Locate every blood parasite and identify its species.
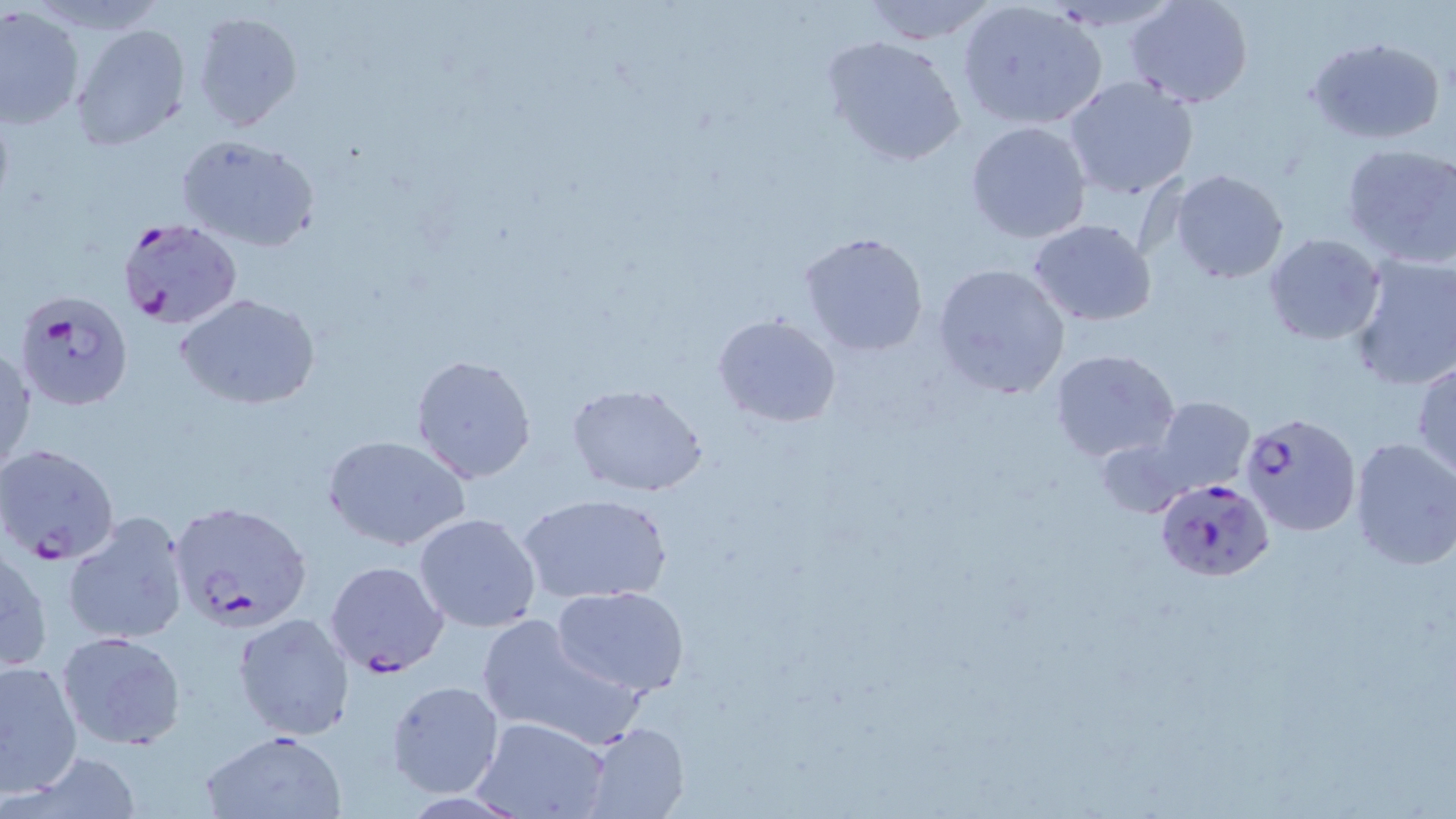
Approximate bounding boxes as named x1/y1/x2/y2 corners in pixels.
Plasmodium falciparum-infected red blood cells: (x1=113, y1=216, x2=243, y2=329), (x1=15, y1=288, x2=135, y2=411), (x1=1240, y1=413, x2=1361, y2=538), (x1=0, y1=442, x2=122, y2=565), (x1=1155, y1=478, x2=1273, y2=582), (x1=168, y1=500, x2=315, y2=635), (x1=324, y1=560, x2=449, y2=678).
No Plasmodium ovale, Plasmodium malariae, Plasmodium vivax, Babesia divergens, or Trypanosoma brucei observed.

Uninfected red blood cell locations: (x1=860, y1=0, x2=998, y2=43), (x1=1124, y1=1, x2=1254, y2=107), (x1=957, y1=4, x2=1105, y2=129), (x1=0, y1=5, x2=85, y2=128), (x1=189, y1=9, x2=303, y2=134), (x1=71, y1=23, x2=190, y2=152), (x1=824, y1=35, x2=967, y2=168), (x1=1305, y1=35, x2=1445, y2=144), (x1=1062, y1=75, x2=1198, y2=200), (x1=965, y1=120, x2=1092, y2=243), (x1=175, y1=133, x2=322, y2=254), (x1=1340, y1=141, x2=1456, y2=270), (x1=1171, y1=169, x2=1289, y2=283), (x1=1028, y1=220, x2=1158, y2=327), (x1=797, y1=231, x2=929, y2=358), (x1=1264, y1=233, x2=1384, y2=344), (x1=1348, y1=253, x2=1456, y2=392), (x1=932, y1=263, x2=1071, y2=400), (x1=175, y1=292, x2=321, y2=409), (x1=711, y1=313, x2=842, y2=427), (x1=1, y1=340, x2=35, y2=480), (x1=1049, y1=349, x2=1181, y2=465), (x1=408, y1=353, x2=538, y2=485), (x1=1411, y1=361, x2=1456, y2=478), (x1=565, y1=382, x2=710, y2=498), (x1=1149, y1=396, x2=1256, y2=497), (x1=323, y1=435, x2=471, y2=553), (x1=1097, y1=436, x2=1195, y2=519), (x1=1347, y1=437, x2=1456, y2=570), (x1=522, y1=493, x2=671, y2=606), (x1=63, y1=511, x2=190, y2=646), (x1=413, y1=513, x2=542, y2=634), (x1=0, y1=543, x2=51, y2=676), (x1=552, y1=585, x2=691, y2=698), (x1=232, y1=612, x2=354, y2=743), (x1=475, y1=613, x2=639, y2=749), (x1=57, y1=631, x2=186, y2=751), (x1=0, y1=657, x2=83, y2=799), (x1=386, y1=680, x2=506, y2=799), (x1=474, y1=716, x2=612, y2=819), (x1=579, y1=721, x2=690, y2=819), (x1=200, y1=728, x2=346, y2=818), (x1=14, y1=751, x2=143, y2=818). Slide-level diagnosis: Plasmodium falciparum. Single field of view. Image is 1456×819 pixels. May-Grünwald-Giemsa-stained preparation. Light microscopy. Thin blood film. Captured at 1000x magnification.